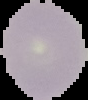

image_type: segmented cell region with the area outside set to black
preparation: thin blood smear
image_size: 88×100 pixels
malaria_status: uninfected